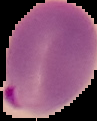
Summary:
  - Image type: segmented cell region with the area outside set to black
  - Malaria status: parasitized
  - Preparation: thin blood film
  - Image size: 97×121 pixels